Report the malaria status of this cell.
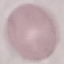

Uninfected.

Summary:
  - Image type: cell patch, automatically extracted from a larger field of view and resized to 64 × 64 pixels
  - Preparation: thin blood film
  - Capture: smartphone camera at the microscope eyepiece
  - Stain: Giemsa